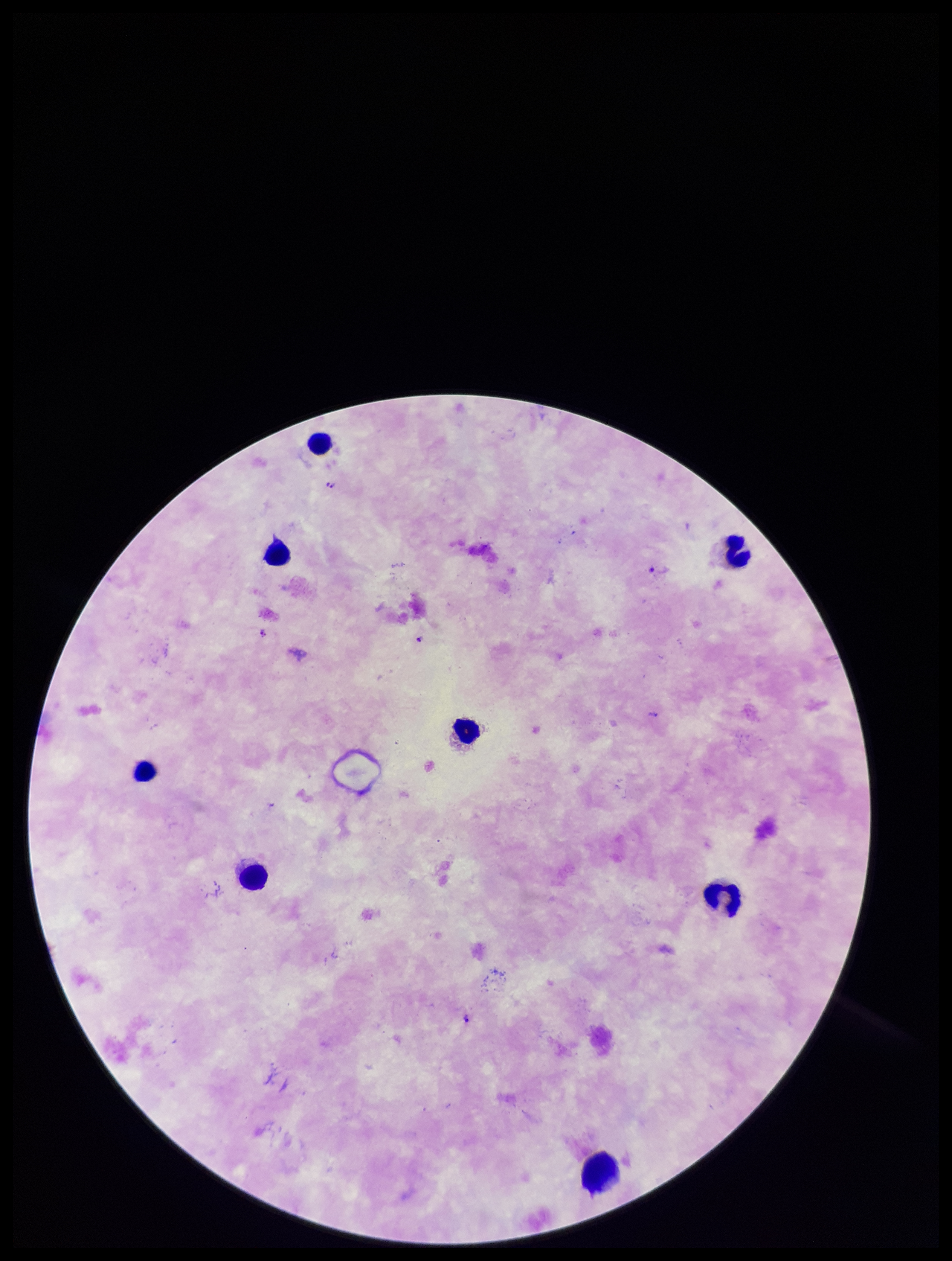
Leukocyte count: 8. Patient malaria status: positive. Species reported for this patient: Plasmodium falciparum. Stained with Giemsa. Preparation: thick smear. One field from this slide. Image is 952×1261 pixels. Plasmodium parasites: detected. Parasite count: 4. Smartphone photograph taken through the eyepiece of a microscope.